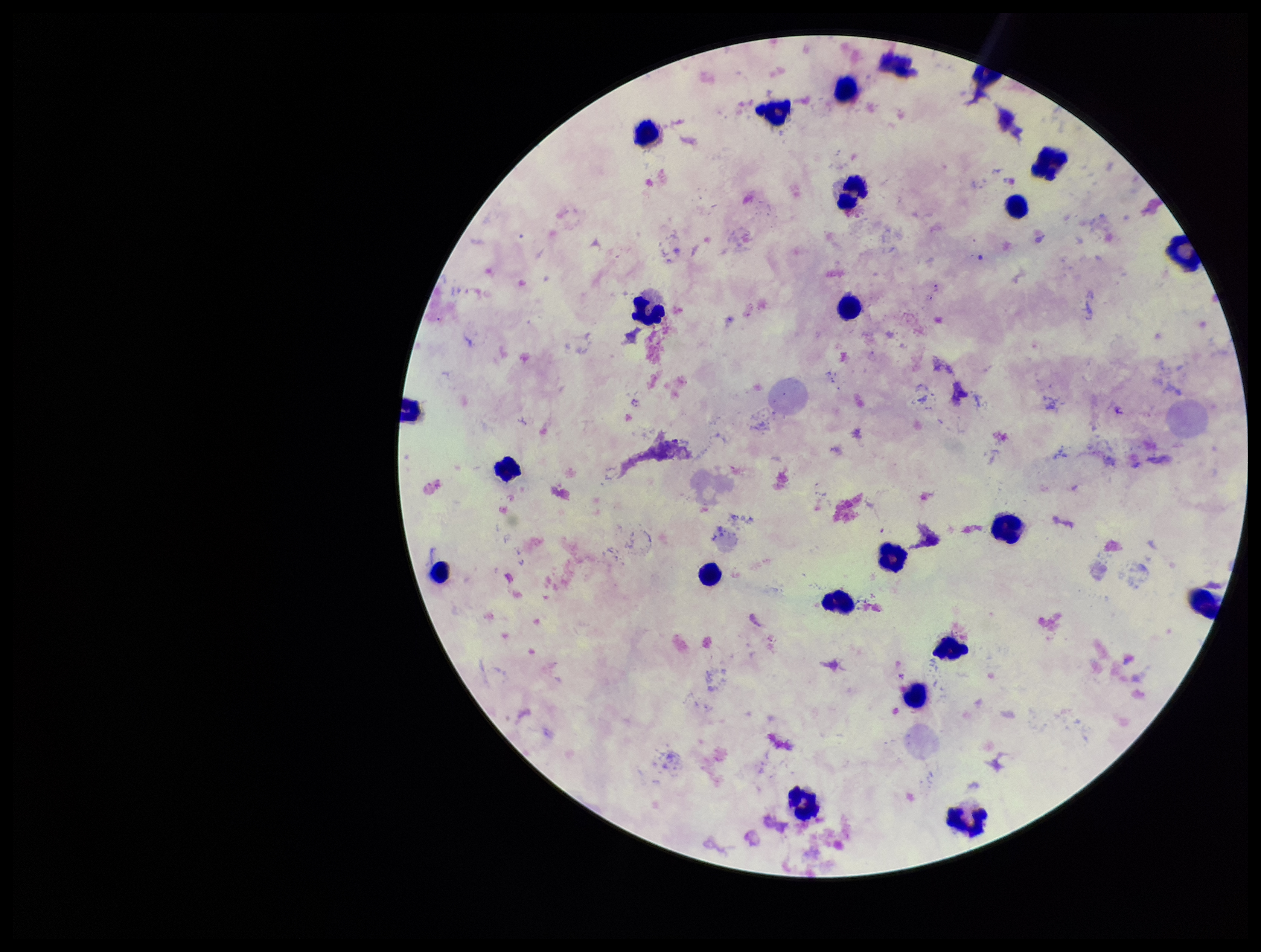
species_reported_for_this_patient: Plasmodium falciparum
parasite_count: 0
preparation: thick
plasmodium_parasites: none seen
capture: smartphone photograph through the microscope eyepiece
leukocyte_count: 23
patient_malaria_status: infected
stain: Giemsa
field_of_view: one from this slide
image_size: 1261×952 pixels